Assess this cell for malaria.
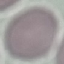
Uninfected.

Thin blood smear. Giemsa stain. Acquired by smartphone through the microscope eyepiece. Cell patch, automatically extracted from a larger field of view and resized to 64 × 64 pixels.